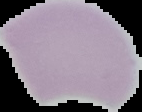
image type = cell region segmented out of the field of view; surrounding area masked to black
image size = 142×112 pixels
malaria status = uninfected
preparation = thin blood smear